Describe the morphology of the red blood cells.
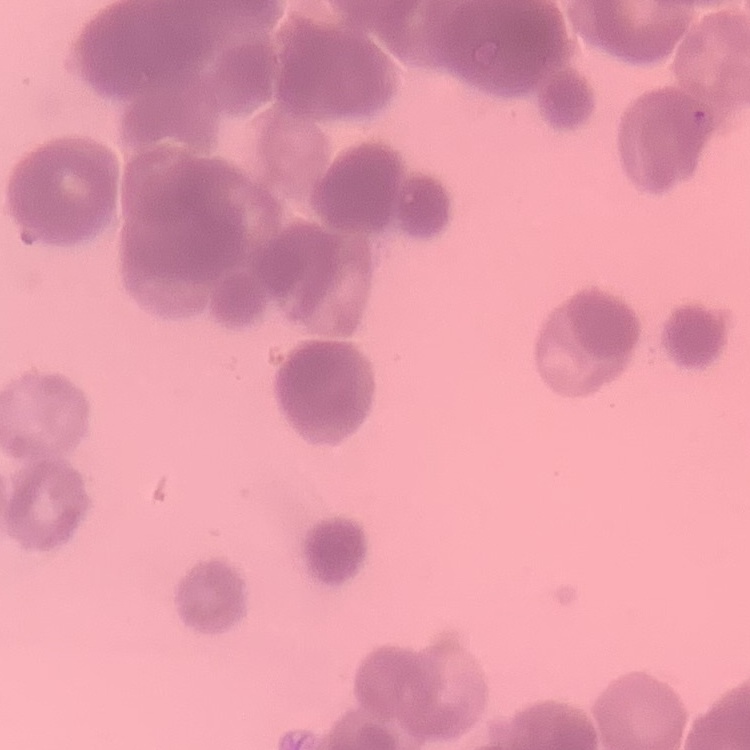
They show rouleaux formation.

Summary:
  - Preparation: thin peripheral smear
  - Stain: Field's or Giemsa
  - Image type: one tile cut from a larger photomicrograph